Evaluate for malaria.
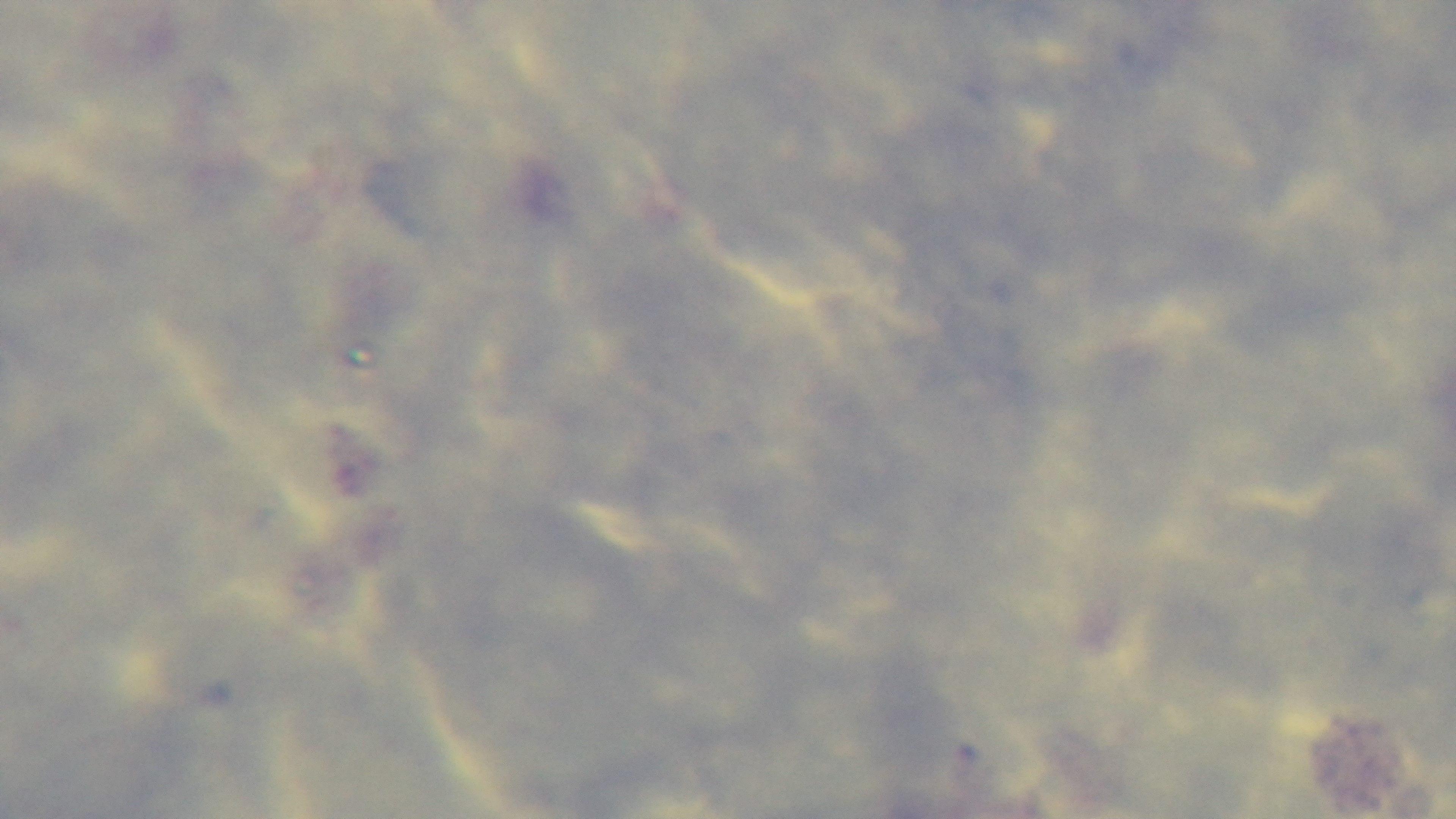

It is uninfected.

One field from the slide. Preparation: thick. 100x oil-immersion objective. Giemsa-stained. Captured with a mounted 4K digital camera. Light microscopy.